Evaluate for parasitized red blood cells.
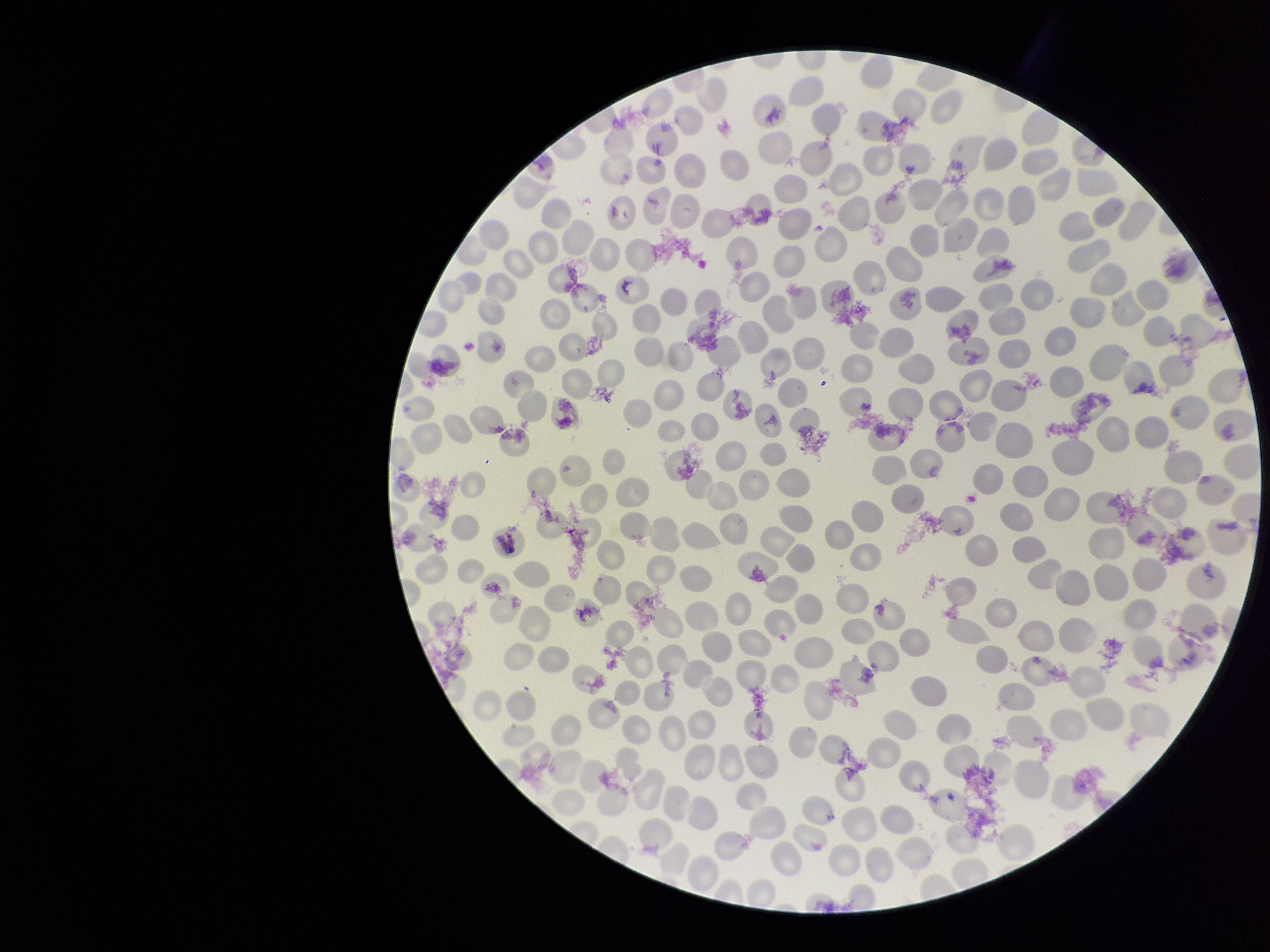
None identified.

Preparation: thin blood smear. Parasitized red blood cell count: 0. Smartphone photograph taken through the eyepiece of a microscope. Image is 1270×952 pixels. Red blood cell count: 269. Stained with Giemsa. Patient malaria status: negative. One field from this slide.